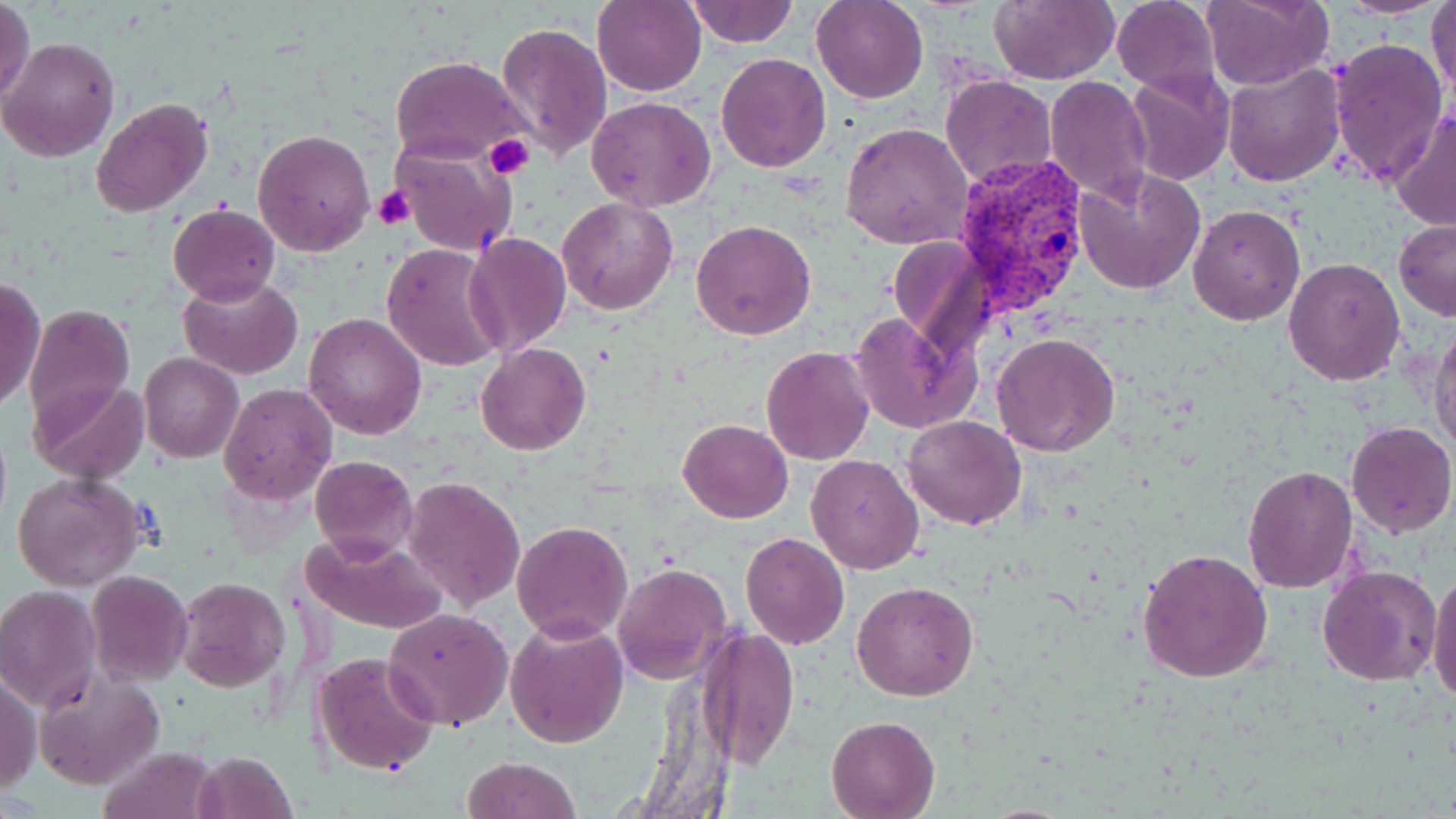

{
  "slide_level_diagnosis": "Plasmodium vivax",
  "image_size": "1456×819 pixels",
  "preparation": "thin blood film",
  "uninfected_red_blood_cell_locations": "approximate bounding boxes as (x1, y1, x2, y2) in pixels: (0, 0, 35, 106), (685, 0, 798, 48), (811, 0, 927, 103), (989, 0, 1116, 87), (1111, 0, 1221, 97), (1201, 0, 1332, 91), (1337, 0, 1447, 17), (1427, 0, 1456, 103), (593, 1, 707, 96), (496, 22, 611, 160), (1, 36, 120, 162), (1329, 37, 1448, 187), (715, 53, 832, 173), (390, 57, 529, 166), (1221, 64, 1344, 187), (1123, 68, 1234, 185), (940, 75, 1057, 188), (1045, 75, 1154, 207), (586, 95, 715, 211), (90, 97, 215, 220), (1390, 104, 1456, 232), (841, 122, 972, 250), (253, 129, 375, 255), (390, 140, 516, 257), (1073, 169, 1205, 295), (556, 197, 678, 316), (169, 203, 280, 305), (1188, 205, 1305, 327), (692, 219, 816, 339), (1394, 219, 1456, 320), (465, 232, 570, 356), (887, 236, 989, 351), (383, 243, 507, 371), (1283, 256, 1407, 387), (180, 275, 302, 379), (1, 277, 45, 414), (24, 304, 135, 429), (847, 310, 980, 435), (304, 312, 428, 440), (1429, 315, 1455, 457), (991, 331, 1122, 458), (476, 342, 590, 456), (761, 348, 874, 465), (139, 352, 243, 463), (33, 379, 146, 484), (219, 385, 337, 504), (903, 415, 1027, 530), (679, 419, 792, 522), (1345, 422, 1455, 537), (806, 453, 924, 574), (310, 455, 418, 563), (1242, 465, 1358, 594), (11, 472, 148, 592), (402, 476, 525, 610), (512, 520, 633, 643), (299, 531, 448, 634), (740, 532, 849, 649), (1137, 547, 1273, 685), (612, 562, 733, 686), (1316, 564, 1441, 686), (1427, 568, 1456, 707), (86, 571, 194, 687), (174, 576, 290, 692), (852, 581, 979, 701), (0, 586, 101, 709), (384, 608, 513, 730), (504, 619, 630, 749), (696, 626, 799, 768), (312, 653, 438, 775), (32, 669, 164, 791), (1, 670, 42, 794), (827, 714, 940, 817), (101, 744, 217, 819), (195, 751, 297, 818), (461, 755, 582, 819)",
  "field_of_view": "one of a larger specimen",
  "plasmodium_vivax_infected_red_blood_cell_locations": "approximate bounding boxes as (x1, y1, x2, y2) in pixels: (951, 154, 1090, 320)",
  "stain": "May-Grünwald-Giemsa",
  "modality": "optical microscopy",
  "platelet_locations": "approximate bounding boxes as (x1, y1, x2, y2) in pixels: (484, 134, 536, 181), (371, 184, 415, 230)",
  "magnification": "1000x"
}